Describe the morphology of the erythrocytes.
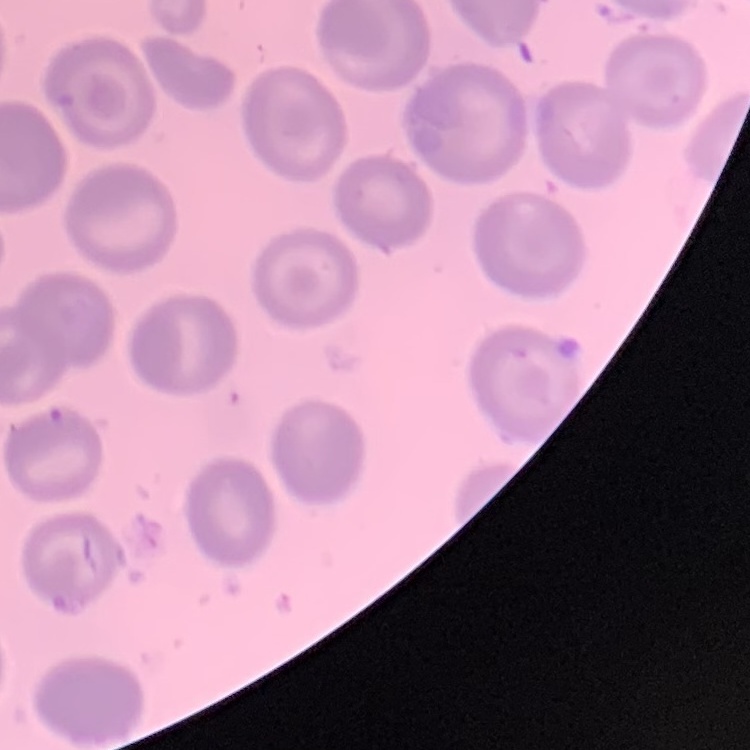

No rouleaux formation.

Summary:
  - Image type: one tile cut from a larger photomicrograph
  - Preparation: thin peripheral smear
  - Stain: Field's or Giemsa